Give the position of every Plasmodium parasite.
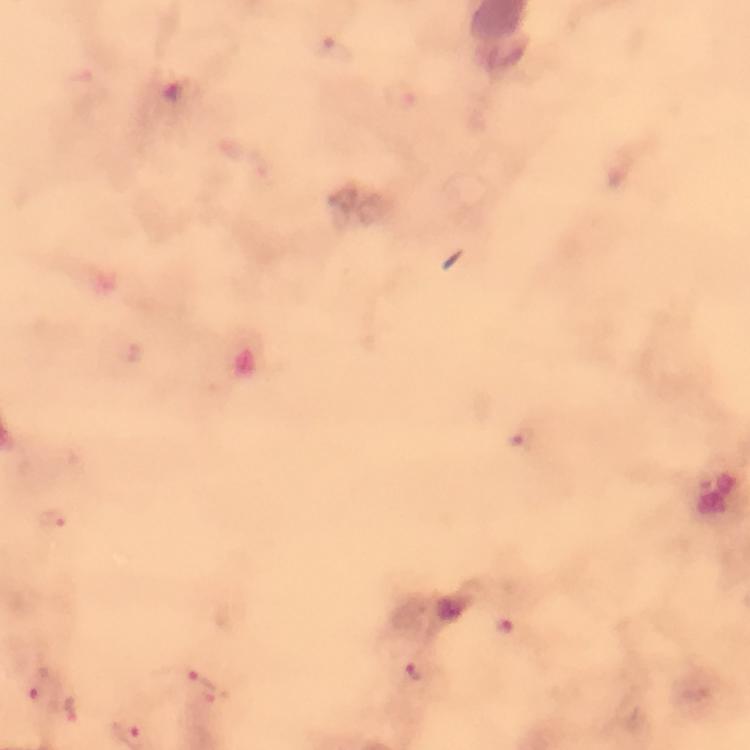
Approximate centers as (x, y) in pixels.
Plasmodium parasites: (521, 437), (55, 518), (506, 625), (418, 674), (37, 685), (201, 685), (70, 710).

From a diagnostic examination for malaria. Image is 750×750 pixels. Giemsa stain. Thick blood film. Cropped region of a single field of view. 100x magnification. Immersion oil was used. Smartphone photograph taken through a microscope.